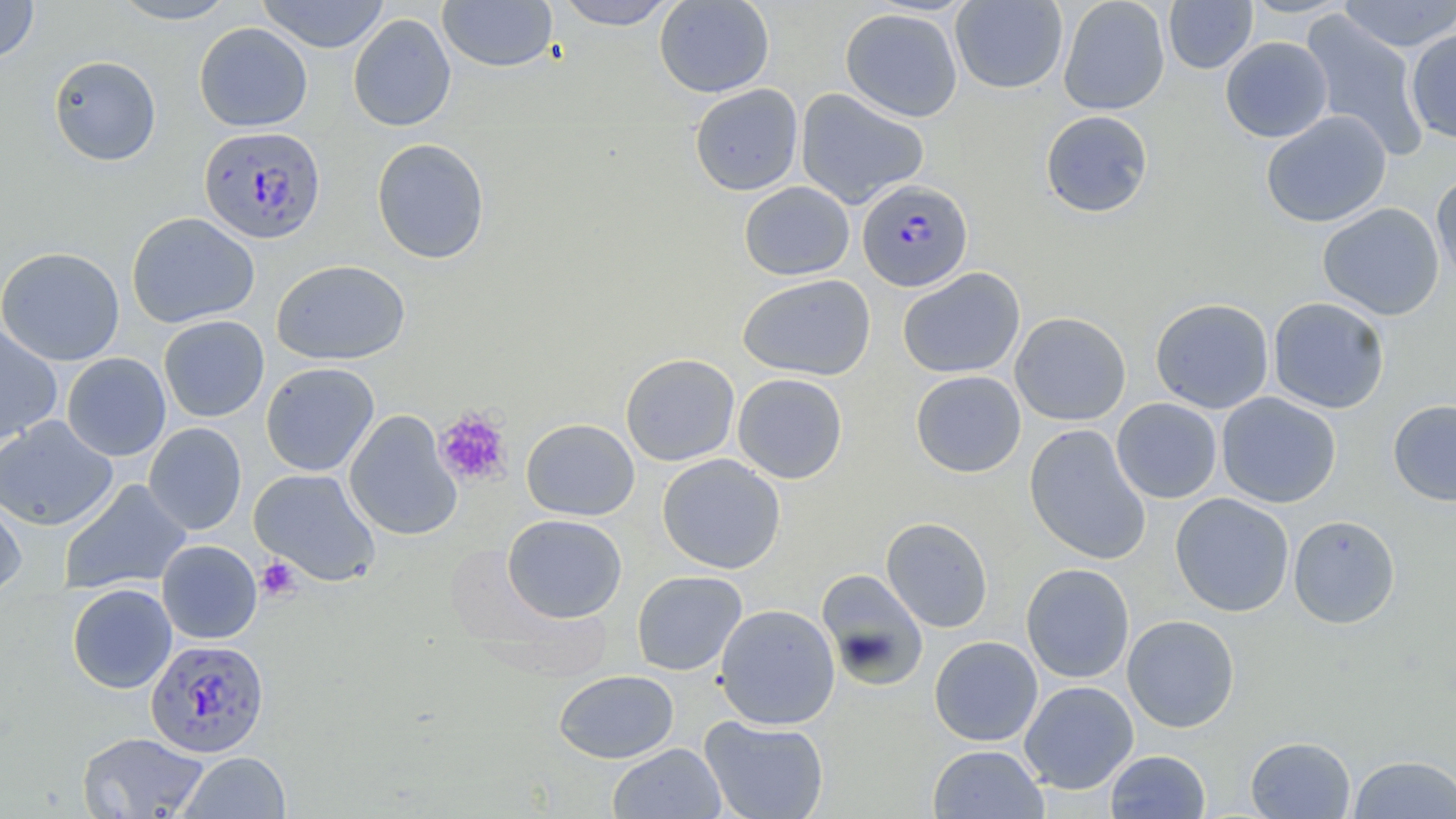

Summary:
  - Coordinate format: approximate bounding boxes as (x1,y1)-(x2,y2) corner pairs in pixels
  - Plasmodium falciparum-infected red blood cell locations: (198,125)-(326,244), (858,179)-(974,293), (143,635)-(269,756)
  - Platelet locations: (434,409)-(512,485), (255,556)-(302,602)
  - Uninfected red blood cell locations: (0,0)-(38,63), (108,0)-(240,25), (256,0)-(391,53), (437,0)-(559,73), (555,0)-(678,30), (654,0)-(774,98), (950,0)-(1068,94), (1058,0)-(1170,115), (1163,0)-(1257,74), (1337,0)-(1456,52), (840,8)-(963,121), (1299,11)-(1430,162), (348,13)-(456,132), (194,22)-(313,132), (1405,28)-(1456,143), (1220,37)-(1333,143), (48,55)-(161,166), (689,84)-(804,196), (795,88)-(929,209), (1040,110)-(1153,217), (1260,110)-(1392,228), (371,137)-(490,264), (1431,171)-(1456,289), (739,181)-(855,280), (1317,202)-(1444,321), (126,211)-(260,329), (0,246)-(126,366), (272,259)-(410,365), (897,267)-(1025,379), (737,273)-(876,380), (1267,297)-(1390,413), (1150,298)-(1274,413), (1010,311)-(1131,426), (159,315)-(269,422), (0,323)-(62,444), (62,352)-(171,461), (620,353)-(740,466), (261,362)-(379,477), (911,370)-(1026,477), (732,373)-(848,483), (1216,392)-(1341,508), (1112,398)-(1223,503), (1388,399)-(1456,506), (344,411)-(462,541), (0,416)-(118,531), (521,418)-(639,520), (144,423)-(246,535), (1024,424)-(1151,565), (657,454)-(785,574), (249,468)-(381,586), (59,479)-(192,595), (1170,493)-(1295,617), (0,494)-(27,594), (502,514)-(627,623), (1288,514)-(1400,629), (881,517)-(994,632), (157,540)-(262,644), (1021,563)-(1135,683), (816,568)-(929,690), (631,570)-(747,676), (66,583)-(177,693), (714,604)-(840,729), (1122,614)-(1240,733), (929,636)-(1043,746), (553,669)-(679,763), (1019,680)-(1139,793), (700,716)-(829,819), (76,731)-(210,818), (1245,736)-(1356,818), (608,743)-(725,819), (928,744)-(1049,819), (1105,750)-(1211,818), (177,751)-(291,818), (1348,754)-(1456,818)
  - Slide-level diagnosis: Plasmodium falciparum
  - Preparation: thin blood film
  - Modality: optical microscopy
  - Field of view: single
  - Image size: 1456×819 pixels
  - Stain: May-Grünwald-Giemsa
  - Magnification: 1000x